Outline each Plasmodium malariae-infected red blood cell.
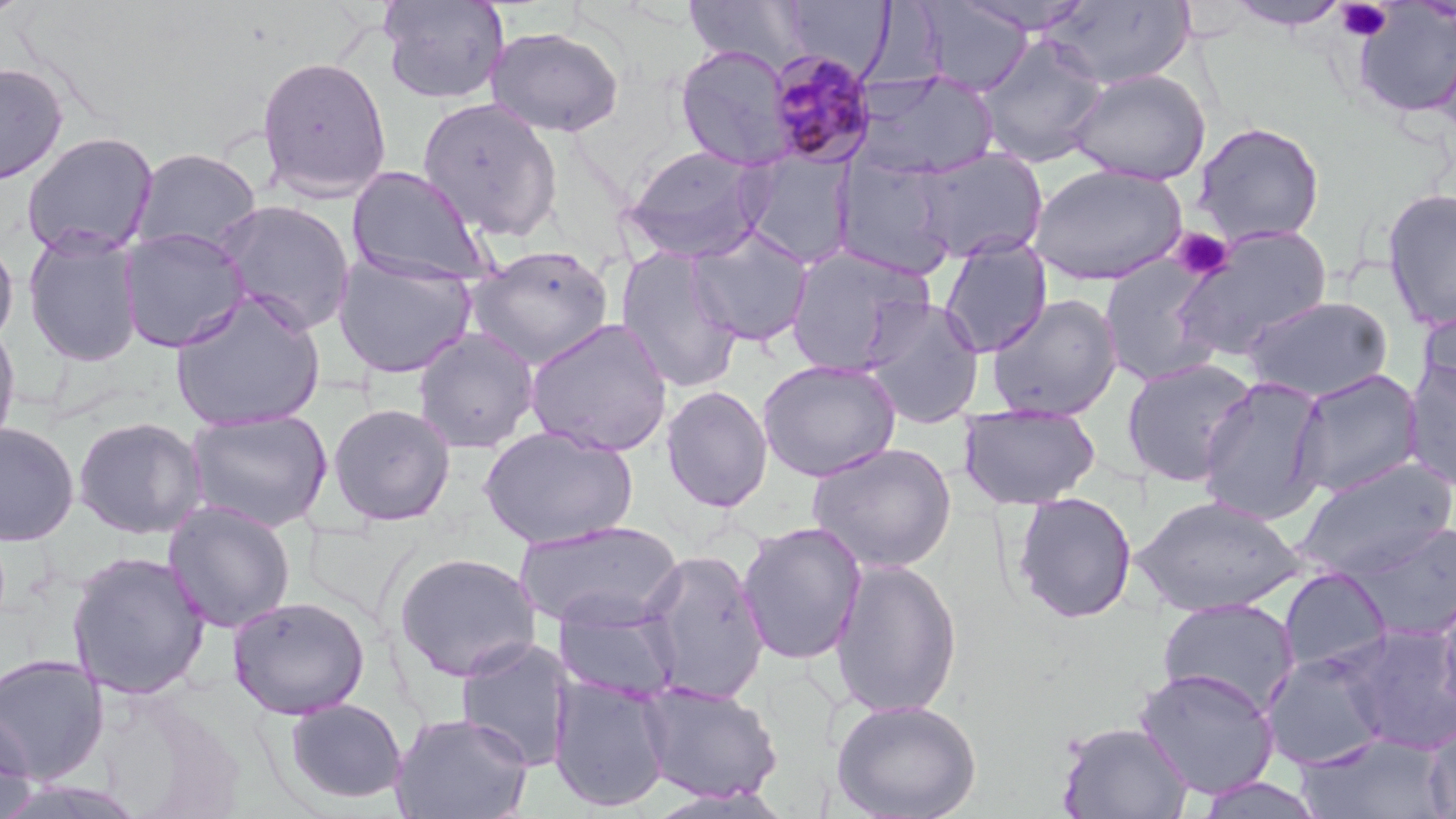

Approximate bounding boxes as named x1/y1/x2/y2 corners in pixels.
Plasmodium malariae-infected red blood cells: (x1=765, y1=50, x2=880, y2=169).

Summary:
  - Platelet locations: (x1=1336, y1=2, x2=1392, y2=42), (x1=1170, y1=227, x2=1235, y2=282)
  - Uninfected red blood cell locations: (x1=683, y1=0, x2=813, y2=73), (x1=952, y1=0, x2=1098, y2=36), (x1=1043, y1=0, x2=1195, y2=90), (x1=378, y1=1, x2=509, y2=104), (x1=780, y1=1, x2=893, y2=77), (x1=1226, y1=1, x2=1353, y2=30), (x1=915, y1=3, x2=1032, y2=95), (x1=1350, y1=4, x2=1456, y2=120), (x1=486, y1=26, x2=625, y2=138), (x1=975, y1=33, x2=1109, y2=168), (x1=675, y1=44, x2=795, y2=171), (x1=256, y1=55, x2=392, y2=202), (x1=0, y1=62, x2=69, y2=185), (x1=1066, y1=68, x2=1211, y2=186), (x1=853, y1=70, x2=999, y2=182), (x1=417, y1=97, x2=563, y2=243), (x1=1192, y1=121, x2=1326, y2=246), (x1=20, y1=131, x2=159, y2=260), (x1=621, y1=145, x2=773, y2=263), (x1=130, y1=147, x2=262, y2=256), (x1=910, y1=147, x2=1048, y2=264), (x1=741, y1=151, x2=856, y2=269), (x1=832, y1=157, x2=959, y2=279), (x1=1029, y1=163, x2=1187, y2=286), (x1=346, y1=166, x2=491, y2=285), (x1=1380, y1=187, x2=1456, y2=332), (x1=215, y1=199, x2=356, y2=336), (x1=1171, y1=224, x2=1334, y2=360), (x1=686, y1=225, x2=813, y2=348), (x1=118, y1=227, x2=251, y2=353), (x1=23, y1=231, x2=144, y2=367), (x1=0, y1=235, x2=18, y2=349), (x1=939, y1=236, x2=1052, y2=357), (x1=465, y1=244, x2=614, y2=369), (x1=783, y1=245, x2=934, y2=377), (x1=615, y1=247, x2=744, y2=394), (x1=332, y1=253, x2=477, y2=378), (x1=1099, y1=257, x2=1222, y2=386), (x1=170, y1=292, x2=326, y2=431), (x1=986, y1=293, x2=1123, y2=421), (x1=1241, y1=295, x2=1395, y2=402), (x1=860, y1=297, x2=986, y2=428), (x1=1418, y1=301, x2=1456, y2=409), (x1=0, y1=318, x2=22, y2=456), (x1=524, y1=318, x2=674, y2=457), (x1=412, y1=328, x2=539, y2=454), (x1=1121, y1=357, x2=1258, y2=486), (x1=757, y1=359, x2=901, y2=481), (x1=1402, y1=359, x2=1456, y2=491), (x1=1289, y1=368, x2=1424, y2=498), (x1=1197, y1=376, x2=1330, y2=525), (x1=660, y1=385, x2=773, y2=513), (x1=327, y1=403, x2=456, y2=526), (x1=958, y1=404, x2=1101, y2=510), (x1=184, y1=408, x2=333, y2=532), (x1=72, y1=416, x2=208, y2=540), (x1=0, y1=423, x2=79, y2=547), (x1=477, y1=425, x2=639, y2=549), (x1=806, y1=442, x2=957, y2=574), (x1=1291, y1=458, x2=1456, y2=582), (x1=1012, y1=491, x2=1138, y2=624), (x1=1132, y1=495, x2=1305, y2=617), (x1=162, y1=500, x2=296, y2=634), (x1=514, y1=520, x2=683, y2=632), (x1=1346, y1=520, x2=1456, y2=643), (x1=737, y1=521, x2=867, y2=665), (x1=638, y1=548, x2=770, y2=705), (x1=66, y1=550, x2=211, y2=700), (x1=393, y1=551, x2=541, y2=682), (x1=830, y1=556, x2=963, y2=719), (x1=1277, y1=566, x2=1393, y2=677), (x1=1433, y1=590, x2=1456, y2=721), (x1=227, y1=595, x2=370, y2=719), (x1=1157, y1=597, x2=1300, y2=716), (x1=553, y1=601, x2=683, y2=704), (x1=1343, y1=622, x2=1456, y2=753), (x1=455, y1=638, x2=573, y2=772), (x1=1262, y1=650, x2=1392, y2=770), (x1=0, y1=654, x2=109, y2=784), (x1=1133, y1=667, x2=1280, y2=799), (x1=549, y1=675, x2=673, y2=812), (x1=638, y1=682, x2=782, y2=803), (x1=283, y1=698, x2=407, y2=805), (x1=831, y1=698, x2=982, y2=819), (x1=0, y1=709, x2=36, y2=819), (x1=390, y1=712, x2=533, y2=818), (x1=1422, y1=715, x2=1456, y2=819), (x1=1056, y1=721, x2=1194, y2=819), (x1=1296, y1=734, x2=1451, y2=819), (x1=1191, y1=775, x2=1328, y2=818), (x1=644, y1=787, x2=792, y2=818)
  - Slide-level diagnosis: Plasmodium malariae
  - Preparation: thin blood film
  - Magnification: 1000x
  - Stain: May-Grünwald-Giemsa
  - Field of view: single
  - Image size: 1456×819 pixels
  - Modality: optical microscopy